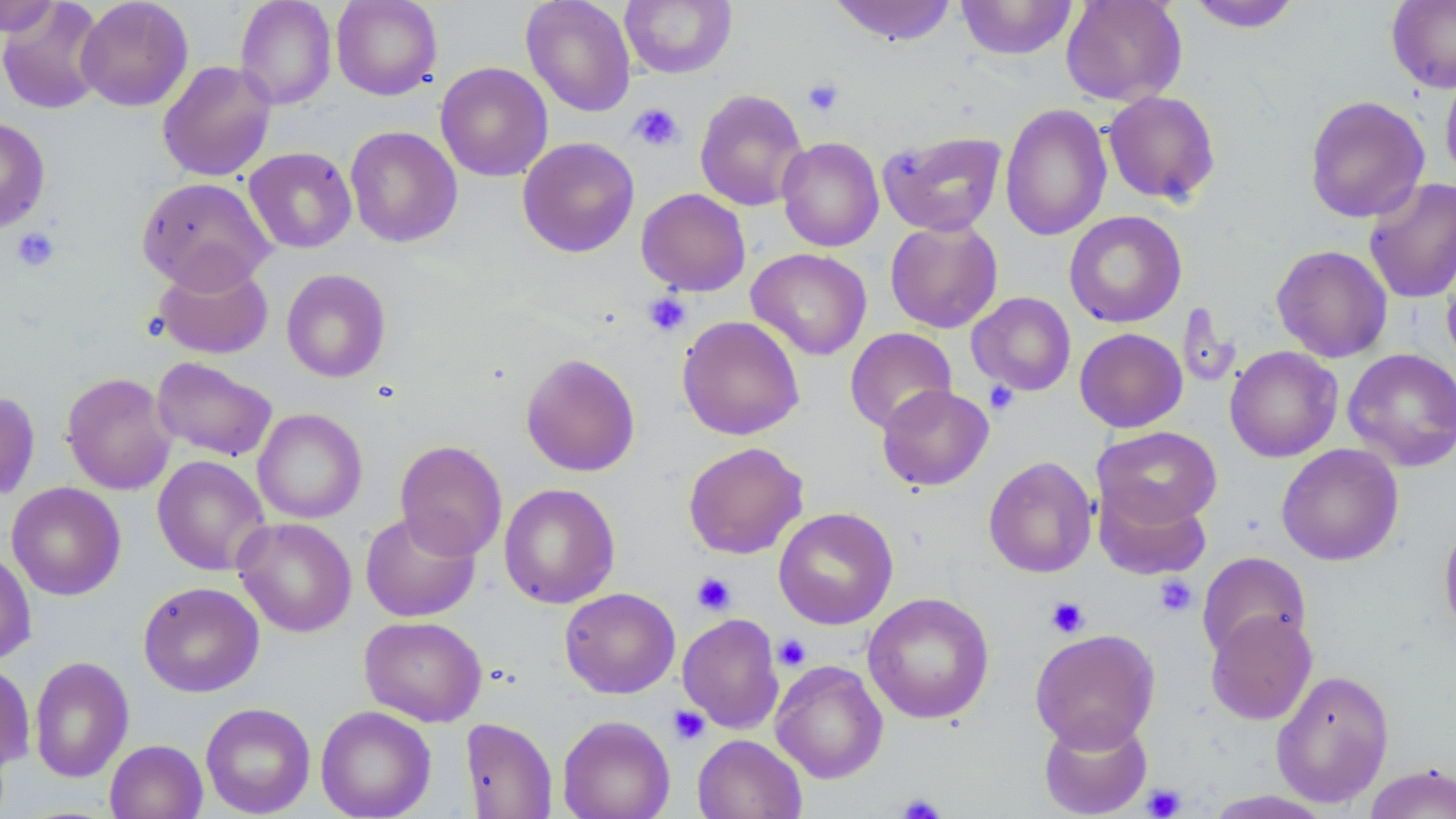

Approximate bounding boxes as [x1, y1, x2, y2] in pixels. Platelet locations: [802, 77, 844, 117], [628, 103, 684, 152], [11, 227, 60, 272], [642, 291, 692, 337], [984, 381, 1019, 414], [691, 572, 736, 616], [1154, 575, 1197, 617], [1046, 597, 1090, 638], [774, 634, 811, 671], [668, 705, 710, 745], [1141, 784, 1187, 818], [896, 792, 947, 819]. Uninfected red blood cell locations: [0, 0, 62, 37], [76, 0, 193, 111], [235, 0, 336, 110], [331, 0, 443, 100], [521, 0, 636, 117], [619, 0, 738, 79], [828, 0, 958, 45], [956, 0, 1077, 60], [1061, 0, 1187, 106], [1184, 0, 1303, 32], [1387, 0, 1456, 93], [0, 1, 108, 115], [157, 60, 276, 182], [435, 61, 553, 182], [1440, 66, 1456, 186], [694, 88, 809, 212], [1102, 90, 1221, 206], [1304, 95, 1429, 222], [999, 103, 1112, 241], [0, 117, 50, 233], [345, 125, 463, 247], [878, 130, 1007, 237], [517, 137, 640, 258], [777, 137, 884, 252], [244, 147, 357, 253], [136, 176, 274, 292], [1364, 177, 1456, 304], [636, 188, 751, 296], [1064, 210, 1186, 328], [885, 219, 1003, 333], [1271, 244, 1393, 362], [747, 248, 872, 360], [1441, 249, 1456, 372], [153, 259, 273, 360], [281, 268, 391, 383], [967, 292, 1076, 396], [1176, 302, 1241, 391], [677, 315, 804, 440], [844, 327, 957, 434], [1074, 328, 1187, 432], [1225, 345, 1343, 462], [1342, 348, 1456, 471], [520, 353, 640, 477], [151, 357, 278, 462], [61, 372, 177, 495], [877, 384, 994, 491], [0, 390, 40, 501], [253, 408, 367, 524], [1094, 426, 1223, 529], [395, 439, 508, 561], [682, 441, 809, 559], [1277, 443, 1404, 566], [152, 455, 270, 576], [983, 455, 1098, 578], [7, 482, 126, 600], [1094, 482, 1212, 581], [499, 483, 620, 609], [773, 506, 898, 629], [360, 510, 481, 622], [233, 517, 357, 636], [1439, 518, 1456, 642], [0, 550, 36, 665], [1197, 551, 1312, 662], [138, 581, 265, 697], [560, 587, 680, 698], [863, 592, 994, 724], [1205, 609, 1317, 725], [677, 613, 784, 733], [360, 616, 487, 726], [1030, 628, 1161, 751], [30, 655, 134, 783], [771, 660, 888, 784], [0, 661, 35, 771], [1271, 669, 1395, 808], [200, 702, 316, 817], [315, 705, 437, 819], [1039, 713, 1153, 818], [557, 715, 675, 819], [460, 718, 558, 819], [692, 734, 807, 819], [105, 740, 208, 819], [1363, 764, 1456, 819], [1203, 790, 1338, 818]. Slide-level diagnosis: negative for blood parasites. Single field of view. Image is 1456×819 pixels. Thin blood smear. May-Grünwald-Giemsa stain. Captured at 1000x magnification. Optical microscopy.